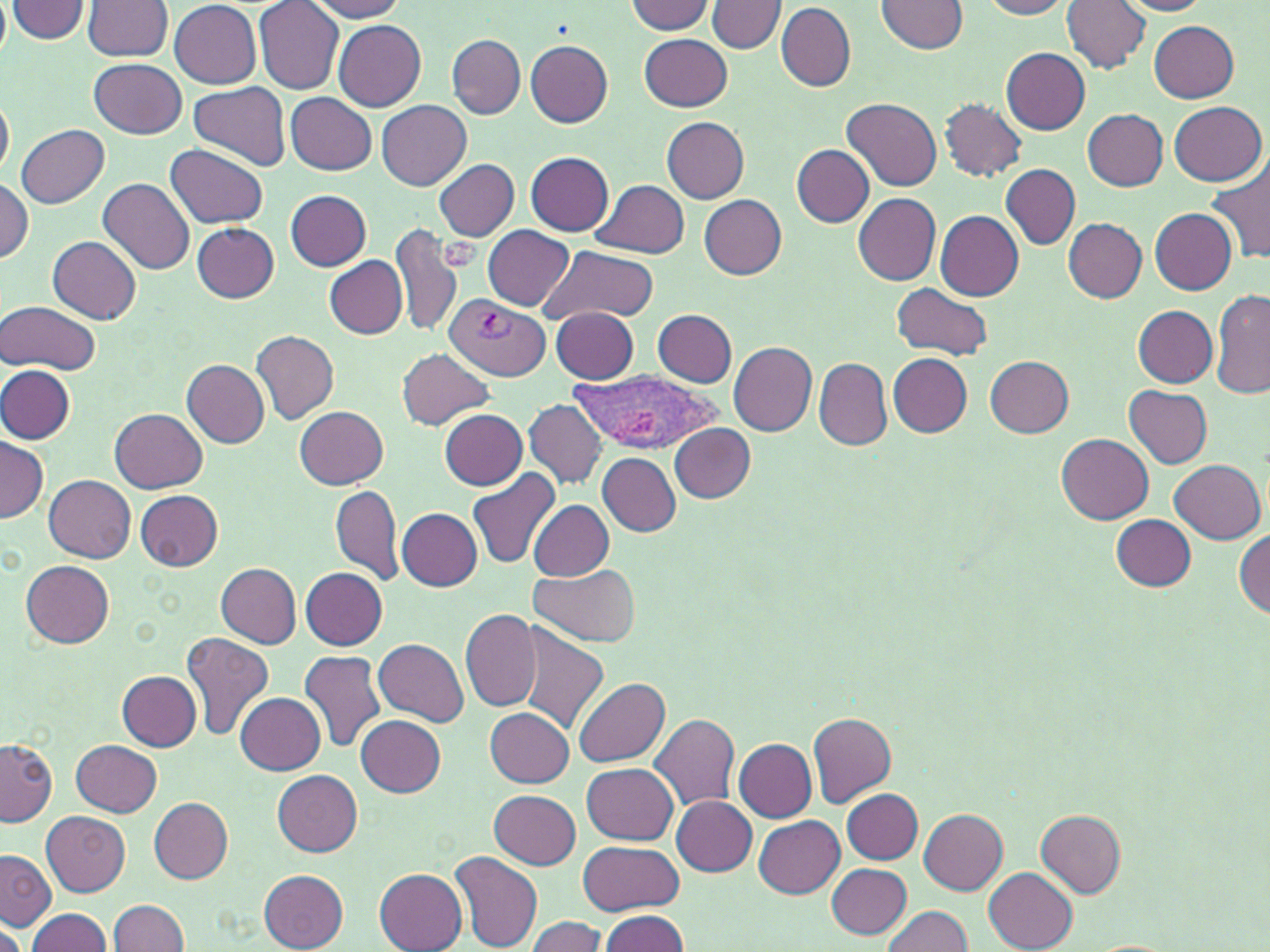
slide-level diagnosis = Plasmodium vivax
image size = 1270×952 pixels
stain = May-Grünwald-Giemsa
magnification = 1000x
uninfected red blood cell locations = approximate bounding boxes as (x1,y1)-(x2,y2) corner pairs in pixels: (7,0)-(90,42), (84,0)-(173,61), (169,0)-(261,88), (308,0)-(410,20), (879,0)-(969,54), (978,0)-(1074,19), (1063,0)-(1149,74), (1116,0)-(1213,16), (254,1)-(343,93), (709,1)-(786,53), (625,2)-(715,35), (775,3)-(855,91), (334,20)-(426,112), (1149,20)-(1239,101), (641,34)-(732,111), (447,35)-(525,118), (524,39)-(613,126), (1000,47)-(1090,134), (90,60)-(186,138), (188,82)-(290,170), (285,92)-(377,174), (0,95)-(13,179), (843,98)-(941,192), (941,99)-(1026,182), (377,101)-(471,190), (1169,101)-(1266,183), (1081,109)-(1169,190), (661,117)-(749,202), (15,124)-(109,207), (167,144)-(269,228), (792,145)-(874,227), (527,152)-(614,235), (434,160)-(520,240), (1208,162)-(1270,263), (524,163)-(687,247), (1001,164)-(1080,249), (0,176)-(34,263), (99,177)-(195,274), (592,179)-(690,259), (286,189)-(370,270), (852,193)-(941,285), (698,194)-(787,277), (1150,208)-(1238,293), (935,211)-(1024,300), (1064,218)-(1147,303), (191,223)-(280,302), (390,223)-(462,339), (483,226)-(574,310), (47,234)-(141,325), (541,244)-(659,326), (325,257)-(407,339), (892,283)-(992,358), (1211,292)-(1270,400), (1,300)-(101,376), (1134,306)-(1217,386), (551,307)-(639,383), (652,310)-(736,386), (251,328)-(338,425), (728,342)-(817,435), (397,348)-(496,430), (887,353)-(973,436), (985,356)-(1074,437), (815,357)-(891,449), (183,361)-(270,448), (0,366)-(75,444), (1123,383)-(1213,468), (523,399)-(607,488), (295,407)-(389,489), (110,409)-(207,493), (439,409)-(528,490), (670,424)-(755,502), (1057,434)-(1154,525), (0,438)-(47,524), (597,454)-(682,536), (1170,459)-(1265,543), (467,468)-(563,569), (45,474)-(136,562), (331,484)-(403,586), (136,489)-(223,571), (530,500)-(615,580), (398,507)-(482,590), (1111,513)-(1196,591), (1234,531)-(1270,617), (21,560)-(115,646), (217,563)-(302,647), (531,565)-(639,647), (301,567)-(388,649), (460,609)-(542,713), (515,623)-(608,735), (181,631)-(276,740), (375,639)-(468,726), (299,648)-(387,755), (117,671)-(203,750), (574,677)-(670,767), (236,692)-(325,774), (486,708)-(573,787), (649,712)-(740,811), (808,713)-(896,809), (357,715)-(447,797), (1,738)-(57,827), (72,739)-(161,817), (734,739)-(816,822), (583,763)-(678,845), (272,769)-(363,855), (490,789)-(581,869), (841,789)-(923,862), (671,796)-(756,876), (150,797)-(234,883), (918,809)-(1007,894), (1035,810)-(1126,897), (42,811)-(130,896), (754,815)-(845,896), (576,841)-(683,915), (0,847)-(57,931), (451,849)-(543,950), (827,862)-(911,938), (374,868)-(467,952), (984,868)-(1077,952), (259,870)-(349,951), (108,898)-(190,951), (882,904)-(973,952), (26,908)-(114,952), (597,910)-(690,952), (523,916)-(608,952), (0,920)-(26,952)
platelet locations = approximate bounding boxes as (x1,y1)-(x2,y2) corner pairs in pixels: (438,236)-(483,268)
modality = optical microscopy
field of view = single
Plasmodium vivax-infected red blood cell locations = approximate bounding boxes as (x1,y1)-(x2,y2) corner pairs in pixels: (444,296)-(550,382), (567,370)-(724,458)
preparation = thin blood film